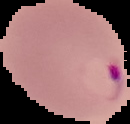

image size = 130×124 pixels
image type = cell region segmented out of the field of view; surrounding area masked to black
result = malaria parasites detected
preparation = thin blood smear